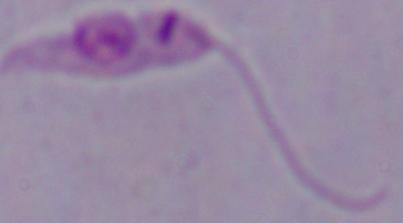

1000x magnification. A Leishmania parasite is seen. Micrograph.